Report the malaria status of this cell.
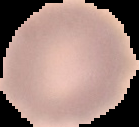
Uninfected.

Image is 139×127 pixels. From a thin blood film. The area outside the segmented cell region is set to black.